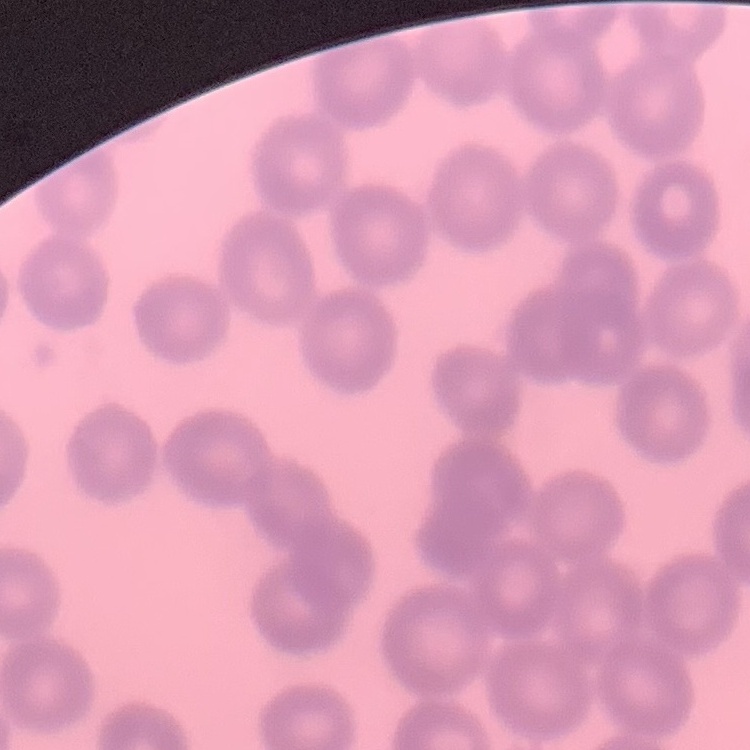

Summary:
  - Erythrocyte morphology: no rouleaux formation
  - Stain: Field's or Giemsa
  - Preparation: thin blood film
  - Image type: one tile cut from a larger photomicrograph